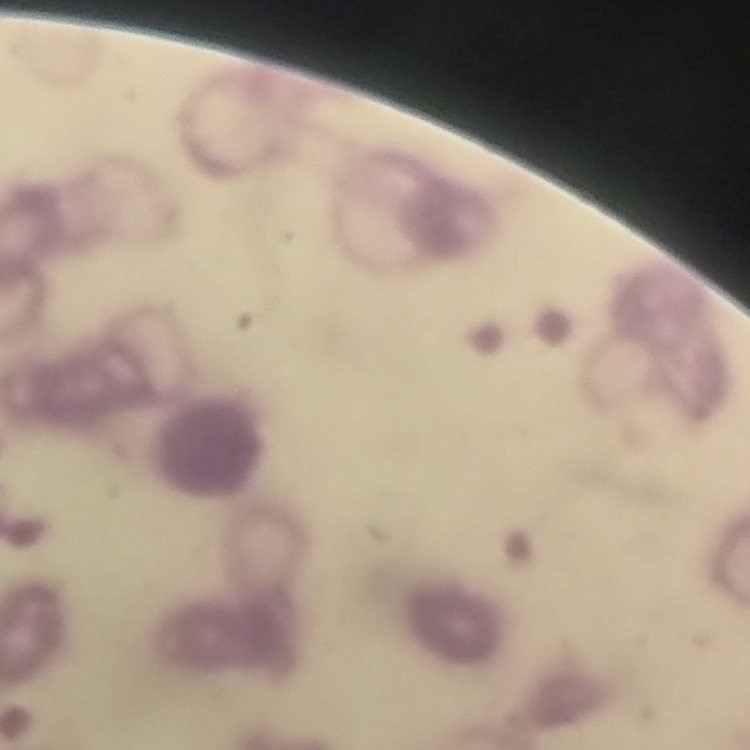
Summary:
  - Erythrocyte morphology: rouleaux formation
  - Image type: one tile cut from a larger photomicrograph
  - Preparation: thin blood smear
  - Stain: Field's or Giemsa